Name the parasite shown.
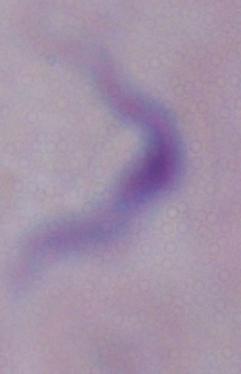

This is a trypanosome.

Summary:
  - Magnification: 1000x
  - Modality: micrograph